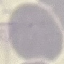

{
  "result": "no malaria parasites detected",
  "stain": "Giemsa",
  "image_type": "cell patch, automatically extracted from a larger field of view and resized to 64 × 64 pixels",
  "preparation": "thin blood smear",
  "capture": "smartphone camera at the microscope eyepiece"
}